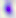
{
  "identification": "Toxoplasma gondii",
  "modality": "photomicrograph",
  "magnification": "400x"
}